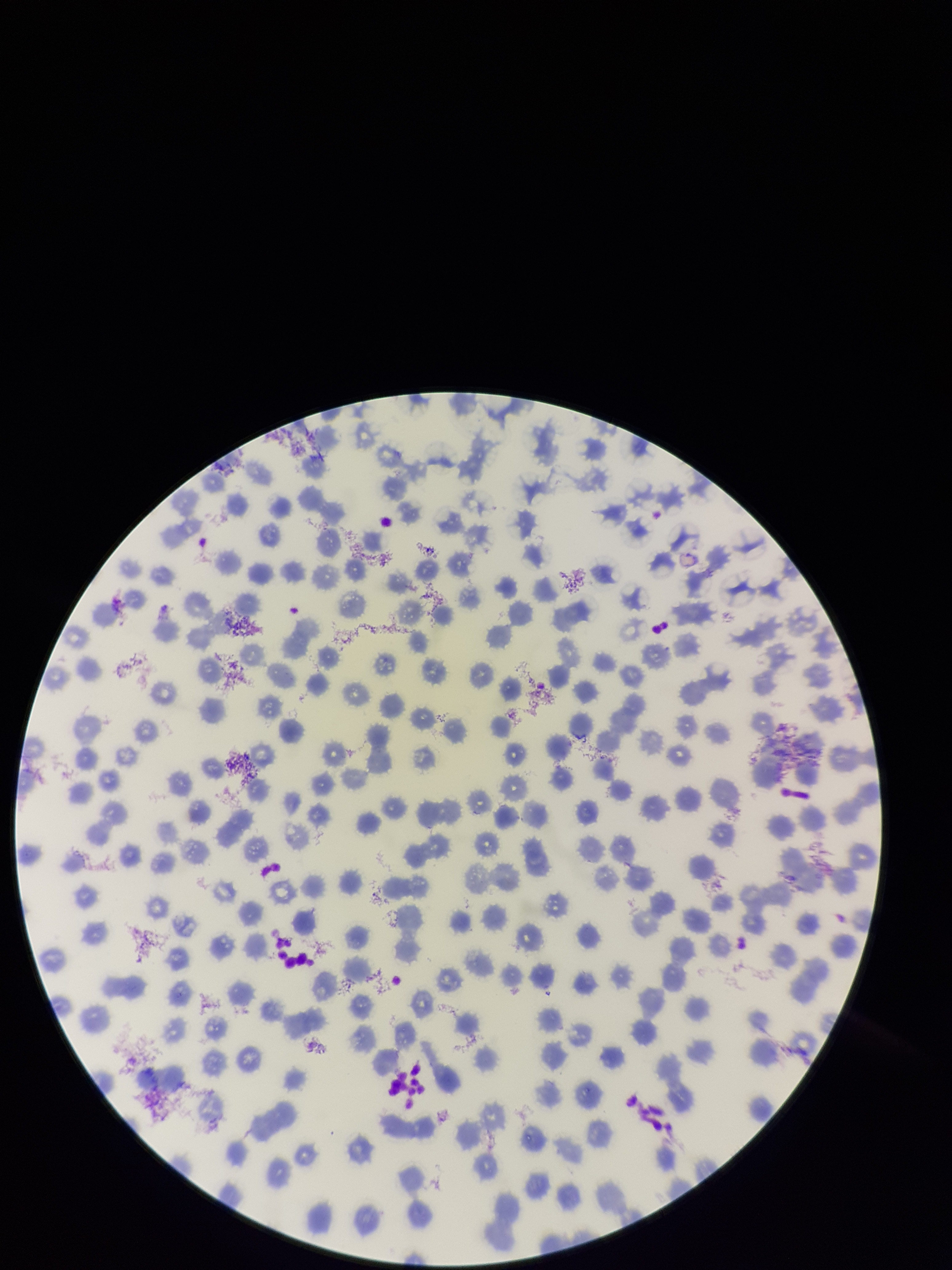
Giemsa stain. Patient malaria status: negative. One field from this slide. Smartphone photograph taken through the eyepiece of a microscope. Image is 952×1270 pixels. Red blood cell count: 262. Parasitized red blood cells: none detected. Preparation: thin blood smear. Parasitized red blood cell count: 0.